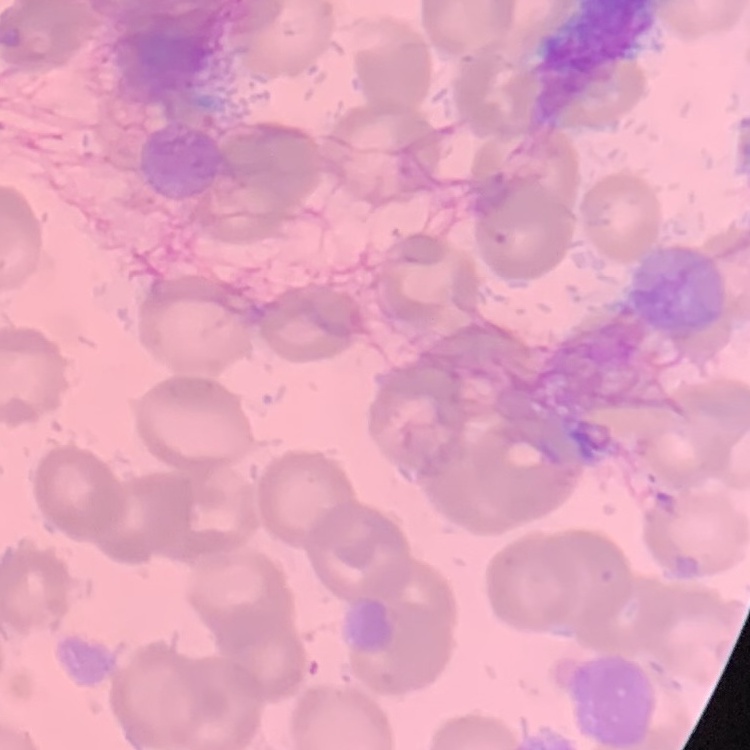
The red blood cells show no rouleaux formation. Square crop of a larger photomicrograph. Field's or Giemsa stain. Thin blood smear.